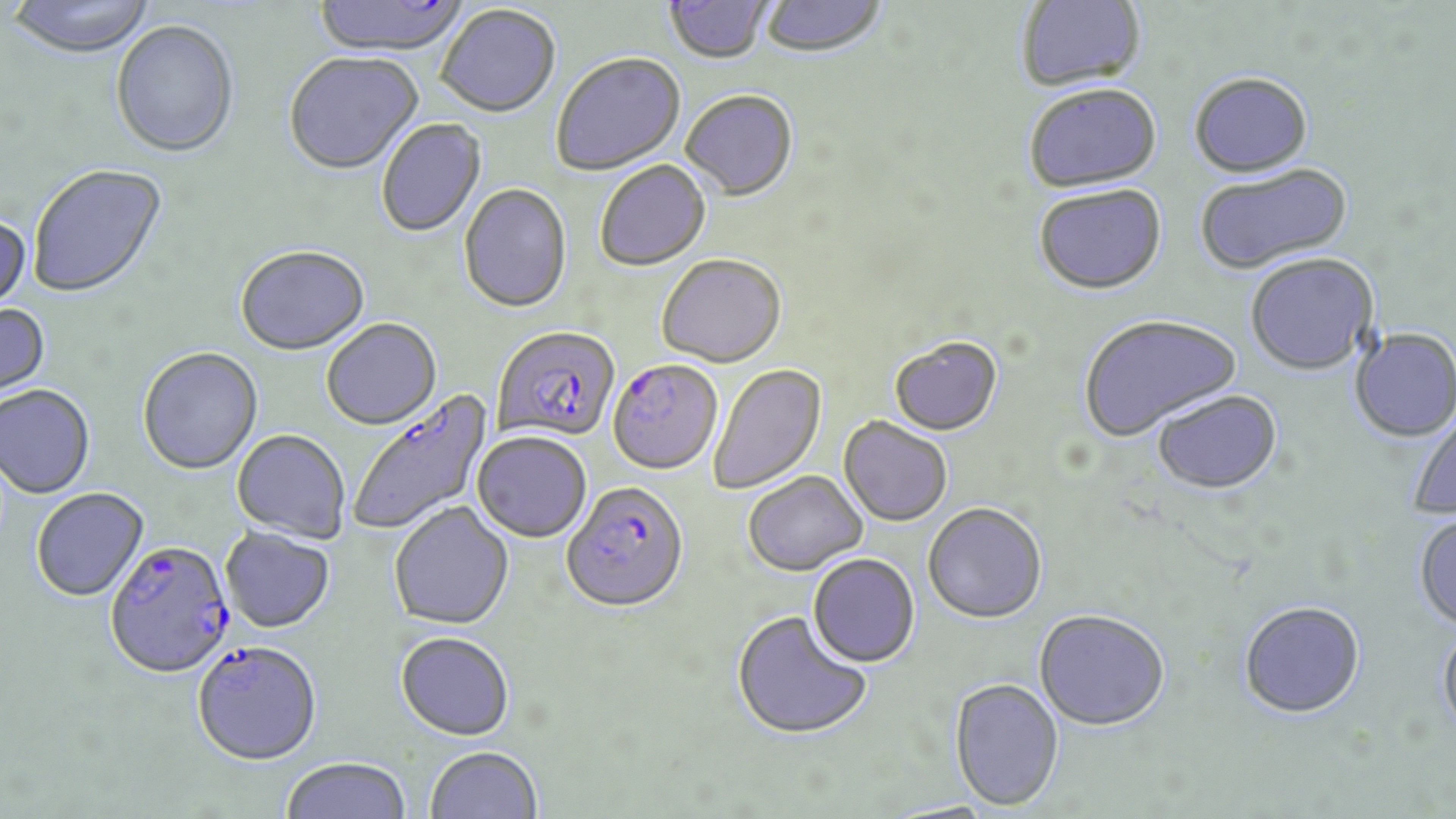
{
  "slide_level_diagnosis": "Plasmodium falciparum",
  "preparation": "thin blood smear",
  "field_of_view": "one of a larger specimen",
  "modality": "optical microscopy",
  "uninfected_red_blood_cell_locations": "approximate bounding boxes as (x1, y1, x2, y2) in pixels: (5, 0, 158, 60), (313, 0, 469, 58), (759, 0, 889, 60), (1016, 0, 1147, 94), (663, 1, 774, 66), (436, 6, 561, 120), (111, 22, 240, 161), (283, 53, 423, 177), (552, 54, 686, 176), (1189, 73, 1313, 179), (1024, 87, 1162, 195), (681, 92, 798, 202), (377, 120, 487, 239), (596, 162, 711, 273), (1195, 164, 1352, 276), (28, 165, 168, 300), (459, 185, 572, 315), (1034, 187, 1167, 297), (0, 213, 33, 316), (235, 247, 370, 357), (1245, 252, 1379, 376), (657, 257, 786, 370), (0, 303, 52, 406), (1079, 314, 1243, 443), (322, 320, 442, 431), (1350, 327, 1456, 443), (888, 339, 1003, 438), (138, 349, 263, 476), (710, 364, 827, 495), (0, 386, 96, 500), (1151, 390, 1282, 495), (1406, 404, 1456, 520), (838, 419, 952, 527), (231, 430, 351, 544), (472, 433, 592, 543), (743, 472, 869, 577), (31, 488, 149, 602), (389, 503, 514, 631), (923, 505, 1048, 626), (1413, 512, 1456, 632), (220, 528, 335, 633), (808, 554, 920, 669), (1238, 600, 1365, 718), (1033, 610, 1170, 732), (732, 611, 872, 741), (1437, 623, 1456, 739), (394, 632, 515, 742), (949, 679, 1064, 812), (424, 746, 543, 819), (280, 758, 411, 819)",
  "magnification": "1000x",
  "image_size": "1456×819 pixels",
  "stain": "May-Grünwald-Giemsa",
  "plasmodium_falciparum_infected_red_blood_cell_locations": "approximate bounding boxes as (x1, y1, x2, y2) in pixels: (493, 326, 621, 445), (606, 360, 723, 477), (347, 390, 495, 538), (561, 484, 689, 616), (104, 540, 235, 680), (191, 642, 323, 766)"
}